Point out each Plasmodium parasite.
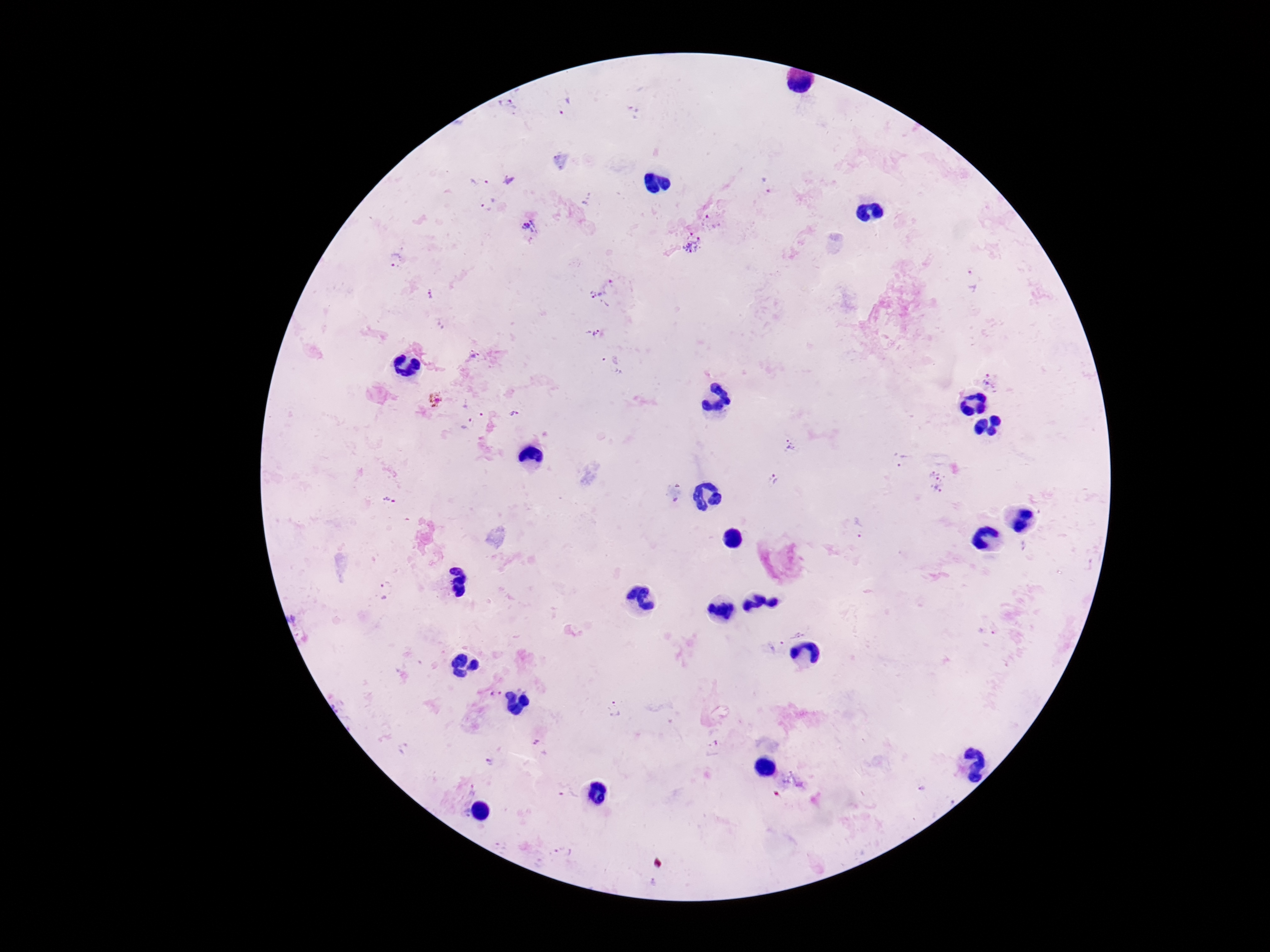

Approximate centers as {x, y} in pixels.
Plasmodium parasites: {507, 105}, {564, 105}, {479, 182}, {767, 186}, {487, 204}, {711, 221}, {529, 225}, {692, 244}, {395, 260}, {974, 280}, {606, 292}, {431, 296}, {596, 334}, {474, 356}, {613, 365}, {989, 380}, {436, 399}, {513, 413}, {469, 422}, {790, 445}, {900, 460}, {774, 478}, {936, 481}, {858, 529}, {385, 588}, {496, 692}, {613, 709}, {537, 742}, {491, 763}, {922, 789}, {565, 853}.

100x magnification. Photographed through the microscope eyepiece with a smartphone camera. Patient malaria status: positive. Single field of view. Image is 1270×952 pixels. Thick peripheral-blood smear. Giemsa stain.